Locate every Plasmodium parasite.
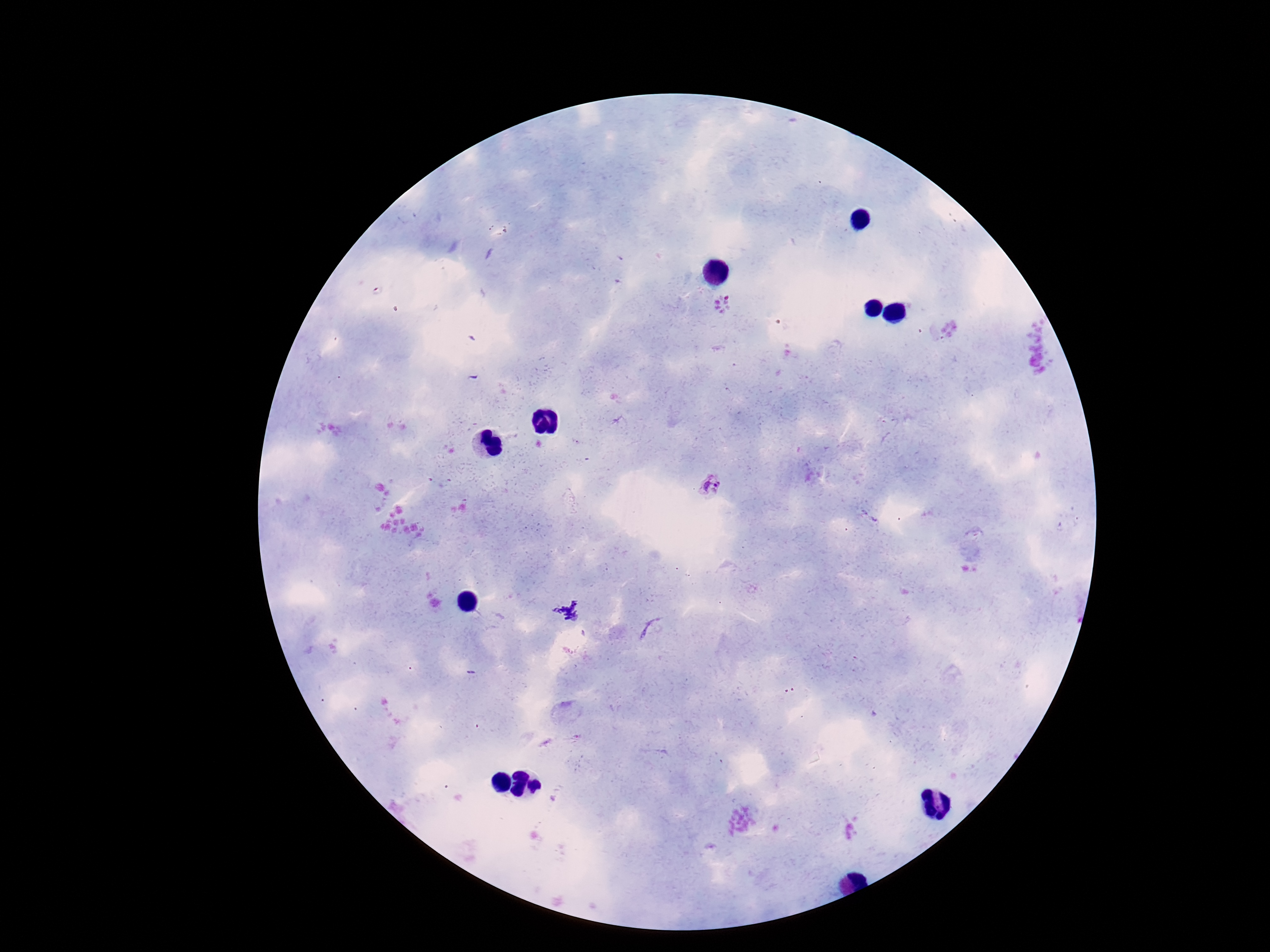
Approximate centers as [x, y] in pixels.
Plasmodium parasites: [714, 485].

Summary:
  - Field of view: single
  - Patient malaria status: positive
  - Magnification: 100x
  - Capture: smartphone camera through the microscope eyepiece
  - Stain: Giemsa
  - Image size: 1270×952 pixels
  - Preparation: thick blood smear